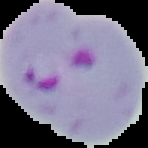
Summary:
  - Image type: cell region segmented out of the field of view; surrounding area masked to black
  - Result: malaria parasites identified
  - Preparation: thin blood smear
  - Image size: 148×148 pixels